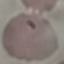

malaria status = parasitized
image type = automatically extracted cell patch, resized to 64 × 64 pixels
stain = Giemsa
capture = smartphone through the microscope eyepiece
preparation = thin blood film